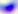

Toxoplasma gondii is shown. Photomicrograph. 400x magnification.